Comment on the morphology of the red blood cells.
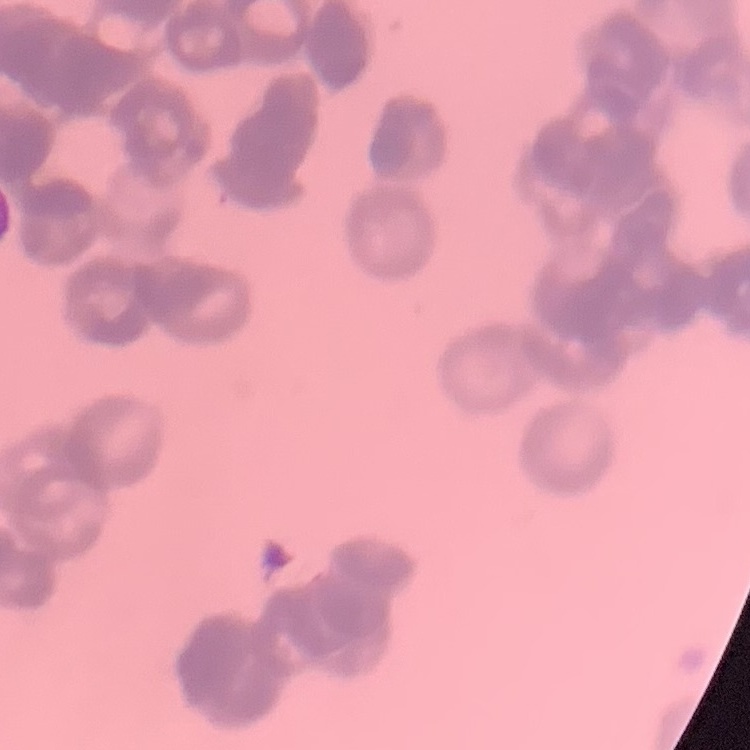

They show rouleaux formation.

One tile cut from a larger photomicrograph. Thin peripheral smear. Field's or Giemsa stain.